Classify this cell by malaria status.
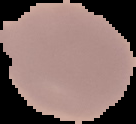
It is uninfected.

From a thin blood film. Image is 136×124 pixels. Segmented cell region on a black background.